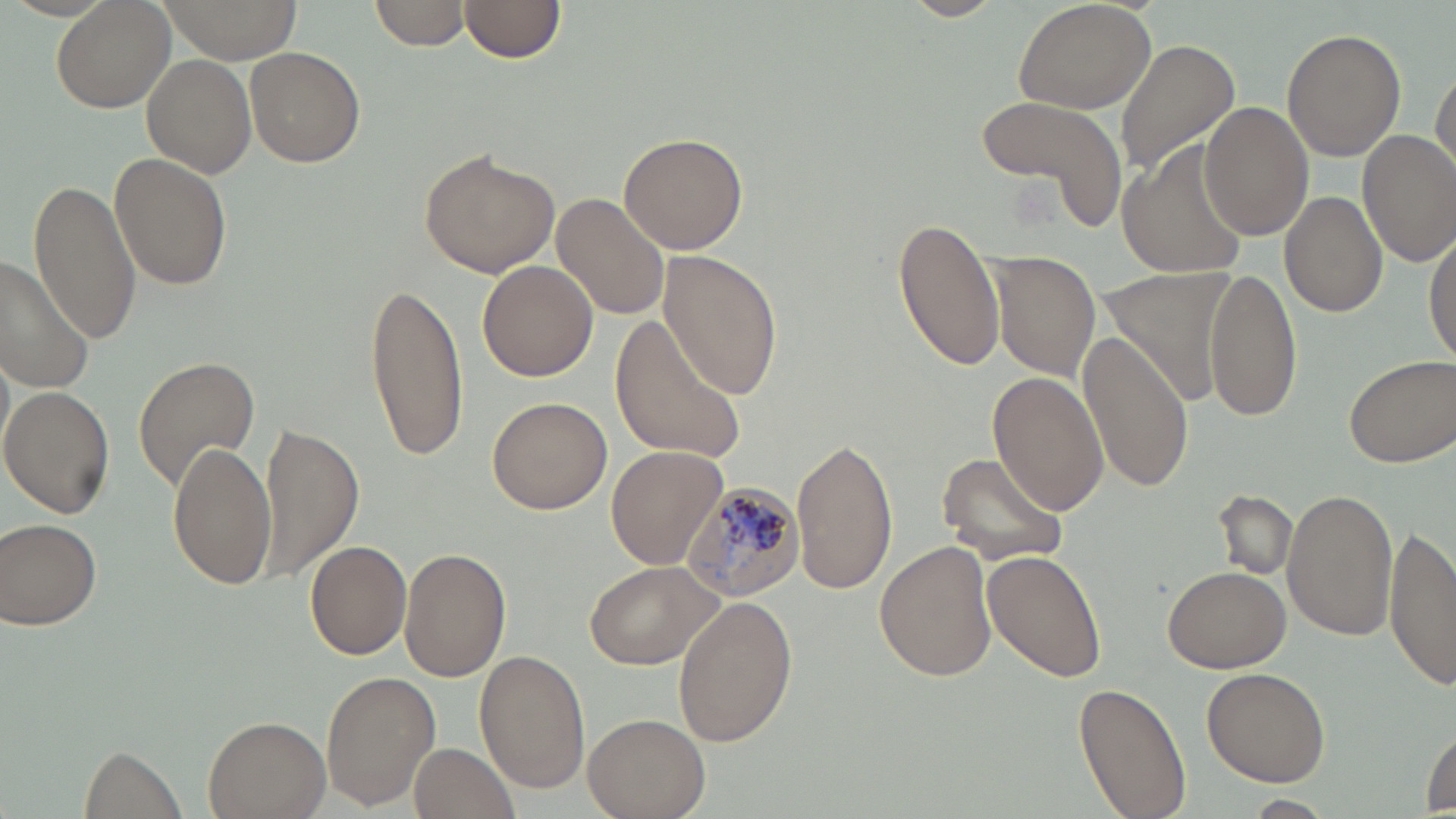
{
  "slide_level_diagnosis": "Plasmodium malariae",
  "magnification": "1000x",
  "stain": "May-Grünwald-Giemsa",
  "plasmodium_malariae_infected_red_blood_cell_locations": "approximate bounding boxes as (x1,y1)-(x2,y2) corner pairs in pixels: (679,483)-(804,600)",
  "image_size": "1456×819 pixels",
  "uninfected_red_blood_cell_locations": "approximate bounding boxes as (x1,y1)-(x2,y2) corner pairs in pixels: (50,0)-(176,112), (155,0)-(302,64), (370,0)-(471,51), (458,0)-(567,63), (1013,0)-(1158,115), (1281,28)-(1406,162), (1114,39)-(1239,177), (245,46)-(365,169), (141,54)-(254,179), (1431,64)-(1456,177), (974,95)-(1130,234), (1198,101)-(1313,241), (1357,130)-(1456,267), (618,131)-(748,255), (1116,146)-(1247,276), (419,147)-(559,279), (108,152)-(234,293), (28,176)-(141,342), (1279,190)-(1389,318), (553,195)-(667,321), (891,213)-(1005,372), (1425,228)-(1456,364), (657,251)-(783,401), (993,252)-(1102,382), (1,257)-(94,392), (477,259)-(598,382), (1102,265)-(1241,402), (1205,266)-(1301,423), (363,278)-(468,461), (612,317)-(750,463), (1076,328)-(1195,493), (1343,353)-(1454,466), (131,355)-(260,491), (989,374)-(1111,514), (1,386)-(115,518), (486,397)-(612,514), (260,423)-(364,582), (789,435)-(898,595), (166,439)-(276,590), (606,445)-(727,571), (936,450)-(1069,565), (1282,487)-(1398,641), (1214,489)-(1298,582), (0,520)-(102,631), (1384,522)-(1456,693), (305,540)-(412,660), (876,540)-(997,683), (400,547)-(511,683), (984,550)-(1107,684), (584,559)-(725,671), (1162,563)-(1292,673), (671,597)-(798,745), (477,650)-(587,793), (1203,668)-(1330,786), (321,670)-(440,810), (1073,682)-(1191,817), (584,711)-(710,818), (205,717)-(329,818), (1421,726)-(1455,814), (411,739)-(520,818), (81,746)-(185,818)",
  "field_of_view": "one of a larger specimen",
  "preparation": "thin blood smear",
  "modality": "light microscopy"
}